Report the malaria status of this cell.
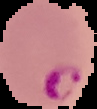
It is parasitized.

Image is 97×109 pixels. The area outside the segmented cell region is set to black. From a thin blood smear.